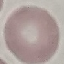
Result: no malaria parasites detected. Thin blood film. Photographed with a smartphone camera at the microscope eyepiece. Automatically extracted cell patch, resized to 64 × 64 pixels. Giemsa stain.